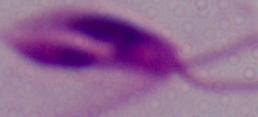

modality = photomicrograph
identification = Leishmania
magnification = 1000x